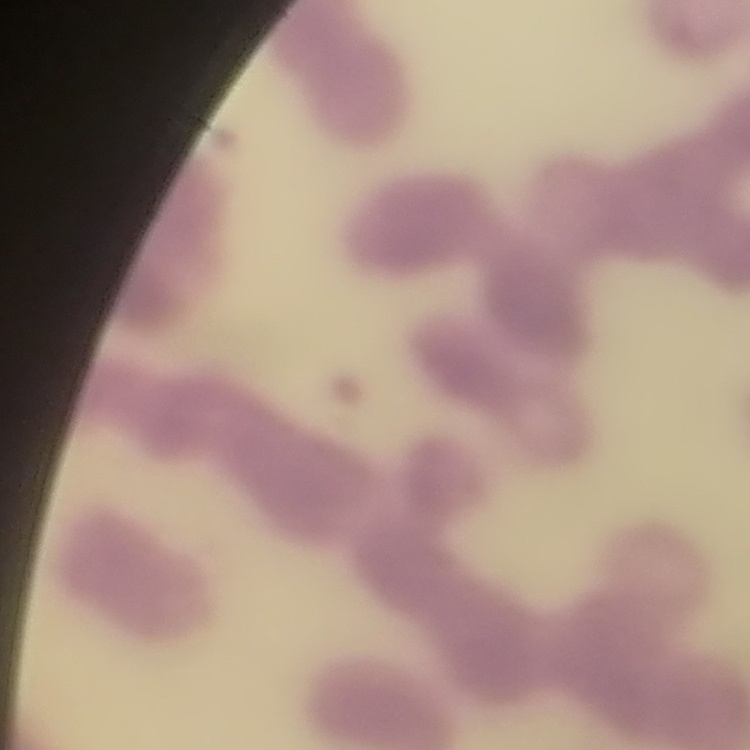

red_blood_cell_morphology: rouleaux formation
stain: Field's or Giemsa
preparation: thin blood smear
image_type: square crop of a larger photomicrograph